Outline each blood parasite and name the species.
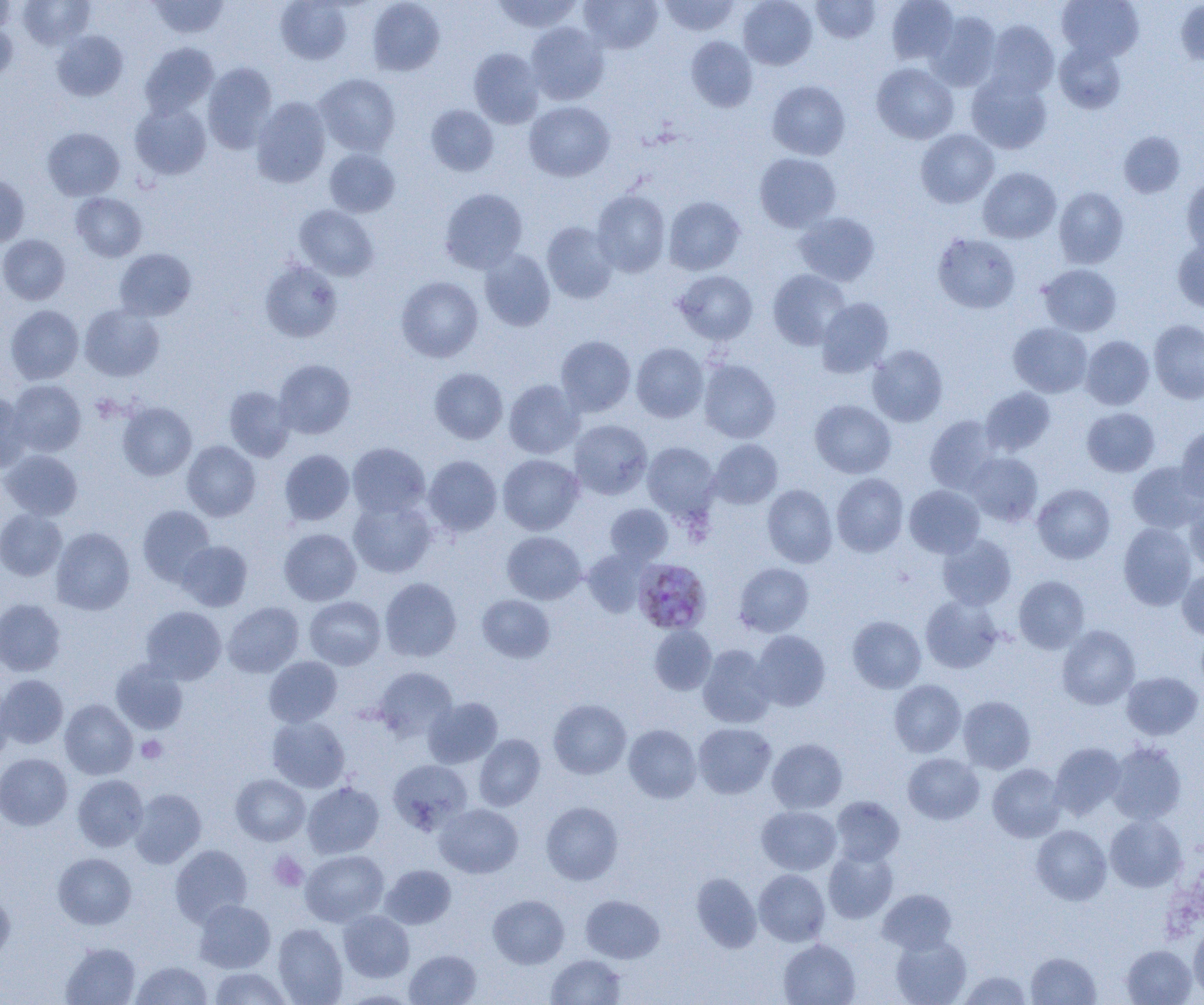

Approximate bounding boxes as (x1,y1)-(x2,y2) corner pairs in pixels.
Plasmodium malariae-infected red blood cells: (633,558)-(711,634).
No Plasmodium falciparum, Plasmodium ovale, Plasmodium vivax, Babesia divergens, or Trypanosoma brucei observed.

slide_level_diagnosis: Plasmodium malariae
image_size: 1204×1005 pixels
modality: optical microscopy
platelet_locations: 'approximate bounding boxes as (x1,y1)-(x2,y2) corner pairs in pixels: (137,735)-(167,763), (268,851)-(308,891)'
uninfected_red_blood_cell_locations: 'approximate bounding boxes as (x1,y1)-(x2,y2) corner pairs in pixels: (18,0)-(95,50), (148,0)-(230,39), (275,0)-(352,64), (491,0)-(583,33), (579,0)-(663,54), (659,0)-(740,36), (738,0)-(817,70), (810,0)-(881,43), (886,0)-(959,65), (1057,0)-(1144,61), (0,1)-(18,34), (367,1)-(445,76), (1176,1)-(1204,67), (928,11)-(1001,91), (0,17)-(17,83), (984,21)-(1059,98), (525,22)-(609,105), (52,30)-(128,101), (686,35)-(758,112), (1054,41)-(1126,113), (140,43)-(218,118), (468,47)-(544,128), (202,62)-(276,153), (872,63)-(959,144), (315,73)-(401,156), (966,74)-(1052,154), (767,80)-(850,160), (251,97)-(331,187), (524,101)-(614,181), (130,103)-(211,179), (425,104)-(499,176), (43,128)-(124,200), (916,129)-(999,208), (1119,131)-(1185,198), (324,148)-(399,217), (754,153)-(841,232), (978,167)-(1061,243), (0,173)-(30,247), (1182,176)-(1204,256), (1054,187)-(1128,269), (440,188)-(528,274), (591,190)-(670,277), (71,192)-(147,262), (664,196)-(745,275), (294,205)-(379,280), (793,212)-(879,286), (541,221)-(619,304), (933,233)-(1021,313), (0,234)-(70,304), (1173,238)-(1204,313), (114,248)-(196,321), (479,249)-(555,331), (259,259)-(342,342), (1039,263)-(1121,336), (768,269)-(851,350), (674,270)-(757,344), (396,276)-(483,362), (816,297)-(894,377), (79,304)-(164,381), (6,305)-(84,384), (1149,319)-(1204,403), (1009,322)-(1092,397), (555,335)-(636,416), (1081,335)-(1154,410), (631,343)-(708,422), (867,344)-(947,426), (274,359)-(355,439), (698,359)-(780,443), (430,368)-(507,444), (503,379)-(584,459), (8,380)-(86,456), (223,385)-(295,461), (981,386)-(1056,456), (0,393)-(33,473), (810,399)-(896,478), (118,401)-(197,480), (1082,407)-(1160,476), (925,415)-(1001,493), (569,420)-(652,499), (1175,426)-(1204,503), (708,439)-(783,509), (182,440)-(260,521), (347,442)-(430,518), (642,442)-(720,521), (1,449)-(83,520), (279,449)-(354,525), (965,452)-(1043,526), (498,454)-(583,535), (423,455)-(502,536), (1127,461)-(1204,534), (831,473)-(908,556), (762,484)-(837,568), (1032,484)-(1115,564), (904,485)-(985,558), (1184,496)-(1204,573), (348,498)-(436,578), (605,504)-(673,566), (137,505)-(215,586), (0,509)-(67,580), (1118,522)-(1197,610), (51,527)-(134,615), (279,528)-(361,605), (501,531)-(587,604), (937,534)-(1016,610), (176,541)-(252,611), (581,548)-(650,617), (734,562)-(814,637), (1177,568)-(1204,641), (1014,575)-(1089,654), (379,577)-(462,662), (477,594)-(555,663), (920,595)-(1003,673), (304,596)-(386,669), (0,599)-(66,676), (223,602)-(304,677), (141,606)-(226,684), (847,616)-(926,693), (649,625)-(716,695), (1057,625)-(1140,709), (750,630)-(831,711), (697,645)-(776,728), (264,656)-(342,727), (111,660)-(188,734), (373,666)-(457,741), (1121,671)-(1202,740), (0,674)-(68,748), (889,680)-(966,757), (0,684)-(14,767), (958,696)-(1035,773), (423,697)-(502,769), (60,699)-(137,779), (548,699)-(631,779), (267,715)-(350,792), (693,723)-(776,798), (624,724)-(701,803), (474,734)-(545,811), (768,738)-(847,814), (1106,741)-(1187,825), (1049,742)-(1126,819), (0,753)-(73,830), (903,753)-(984,824), (388,759)-(472,834), (903,759)-(1066,831), (987,763)-(1066,842), (231,773)-(310,845), (73,774)-(149,851), (302,782)-(384,858), (129,788)-(206,868), (831,796)-(904,866), (541,801)-(623,885), (434,803)-(523,878), (757,805)-(842,875), (1105,814)-(1186,892), (1031,825)-(1111,905), (170,845)-(252,926), (823,848)-(898,923), (301,850)-(388,926), (53,852)-(136,929), (380,864)-(456,929), (754,869)-(830,946), (691,872)-(762,953), (0,889)-(15,963), (878,889)-(956,954), (488,894)-(569,969), (580,895)-(664,963), (194,899)-(275,972), (338,910)-(414,982), (273,923)-(348,1004), (1189,924)-(1204,1000), (890,935)-(971,1005), (778,939)-(860,1005), (60,942)-(141,1005), (1121,945)-(1197,1005), (405,950)-(481,1005), (1026,952)-(1101,1004), (546,954)-(626,1004), (131,960)-(212,1005), (208,967)-(293,1005), (958,971)-(1032,1004), (340,989)-(420,1004)'
preparation: thin blood film
magnification: 1000x
field_of_view: one of a larger specimen